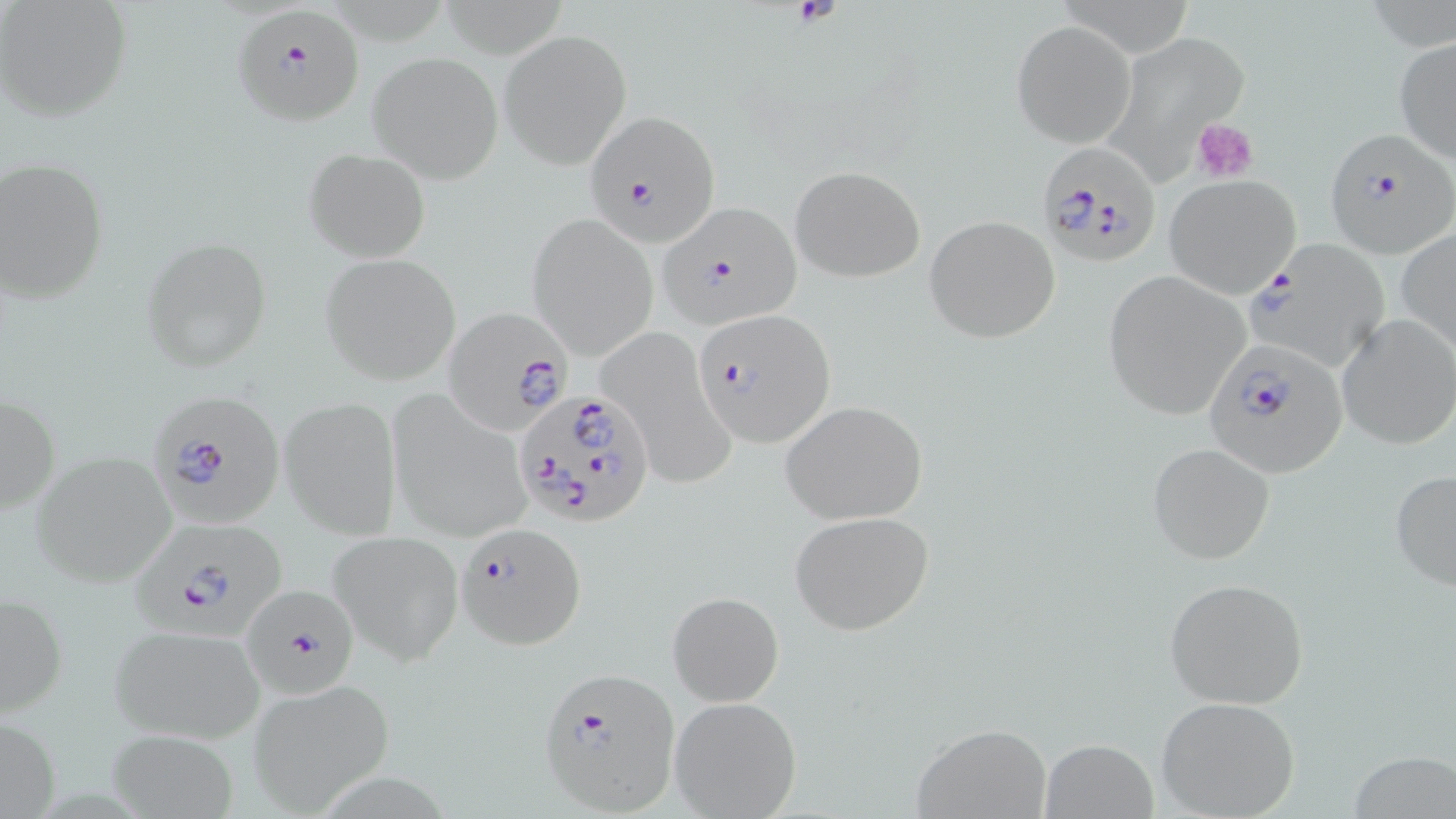

Plasmodium falciparum-infected red blood cell locations = approximate bounding boxes as (x1,y1)-(x2,y2) corner pairs in pixels: (231,3)-(363,127), (582,109)-(721,247), (1320,133)-(1453,261), (1037,141)-(1162,270), (656,201)-(806,331), (1247,240)-(1391,372), (444,308)-(574,435), (693,309)-(835,448), (1202,337)-(1345,477), (147,387)-(288,529), (517,387)-(655,531), (129,517)-(289,639), (455,521)-(587,650), (239,582)-(363,700), (534,668)-(681,814)
slide-level diagnosis = Plasmodium falciparum
preparation = thin blood film
stain = May-Grünwald-Giemsa
platelet locations = approximate bounding boxes as (x1,y1)-(x2,y2) corner pairs in pixels: (1193,120)-(1259,184)
magnification = 1000x
field of view = single
image size = 1456×819 pixels
uninfected red blood cell locations = approximate bounding boxes as (x1,y1)-(x2,y2) corner pairs in pixels: (1,2)-(132,122), (1013,21)-(1135,147), (501,30)-(630,167), (1394,36)-(1456,163), (367,52)-(501,182), (304,147)-(430,263), (0,160)-(109,302), (790,165)-(925,281), (1165,176)-(1299,296), (527,216)-(658,359), (925,216)-(1060,342), (1396,226)-(1456,354), (143,237)-(268,371), (318,253)-(460,385), (1103,271)-(1251,420), (1335,314)-(1455,450), (597,324)-(734,489), (1,389)-(59,521), (385,390)-(534,544), (280,396)-(402,538), (781,400)-(927,525), (1148,443)-(1275,565), (30,451)-(177,587), (1389,467)-(1456,594), (788,510)-(933,636), (328,529)-(464,666), (1163,577)-(1310,710), (1,591)-(67,718), (668,591)-(783,707), (108,623)-(268,745), (248,679)-(395,813), (669,695)-(801,819), (1155,696)-(1300,819), (910,726)-(1053,817), (102,728)-(242,818), (1038,736)-(1160,819), (1350,749)-(1455,819)
modality = optical microscopy